Point out each Plasmodium parasite.
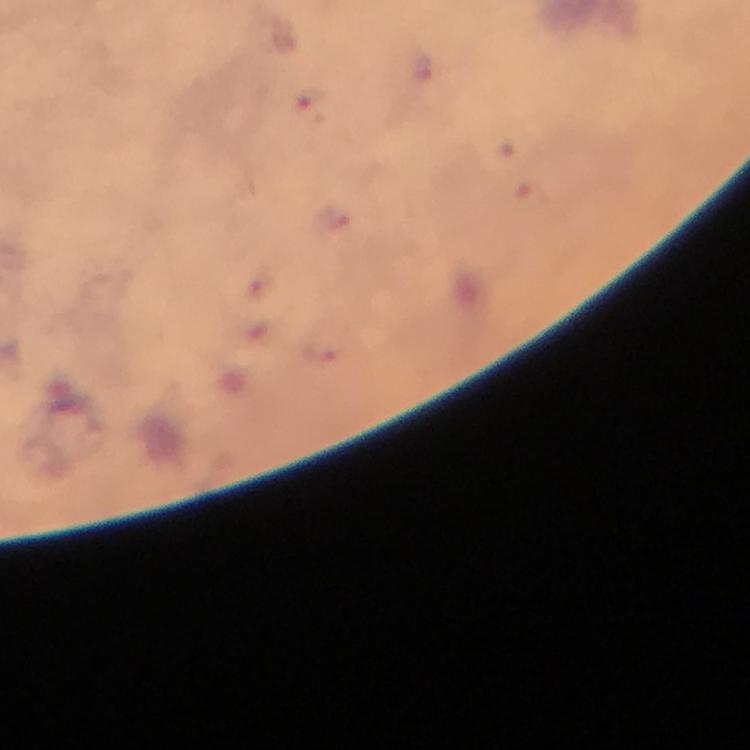
Approximate centers as (x, y) in pixels.
Plasmodium parasites: (312, 105).

Immersion oil was used. Smartphone photograph taken through a microscope. 100x magnification. A crop from one field of view. From a malaria diagnostic workup. Image is 750×750 pixels. Giemsa stain. Thick blood film.